State the blood parasite species.
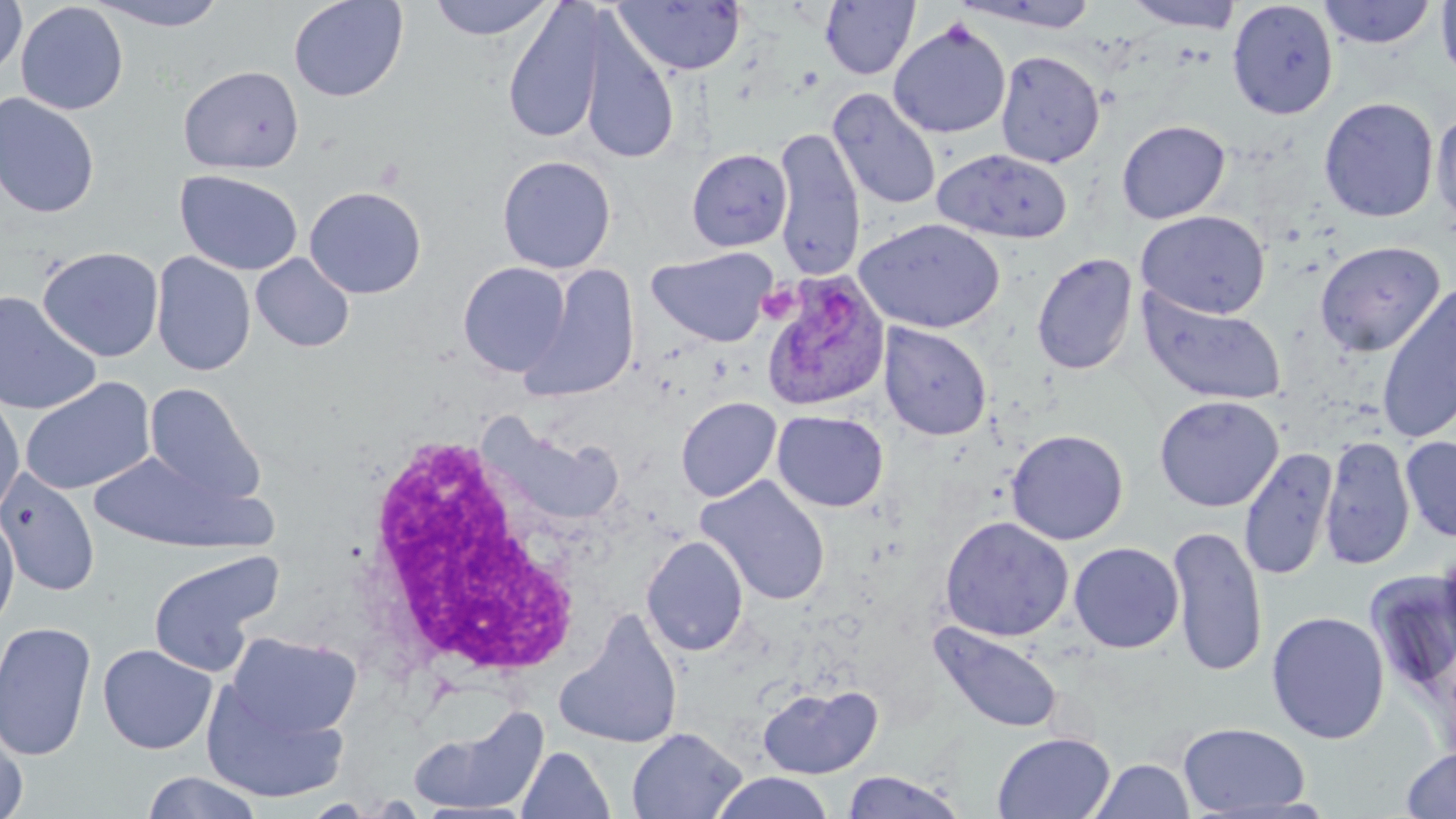

Plasmodium ovale.

{
  "magnification": "1000x",
  "modality": "optical microscopy",
  "field_of_view": "single",
  "preparation": "thin blood film",
  "stain": "May-Grünwald-Giemsa",
  "uninfected_red_blood_cell_locations": "approximate bounding boxes as named x1/y1/x2/y2 corners in pixels: (x1=0, y1=0, x2=27, y2=81), (x1=89, y1=0, x2=230, y2=32), (x1=288, y1=0, x2=409, y2=102), (x1=427, y1=0, x2=556, y2=40), (x1=612, y1=0, x2=746, y2=76), (x1=1123, y1=0, x2=1243, y2=31), (x1=1318, y1=0, x2=1436, y2=49), (x1=15, y1=1, x2=129, y2=116), (x1=820, y1=1, x2=920, y2=80), (x1=954, y1=1, x2=1101, y2=33), (x1=1227, y1=1, x2=1338, y2=119), (x1=1435, y1=1, x2=1456, y2=84), (x1=502, y1=2, x2=608, y2=145), (x1=578, y1=15, x2=681, y2=166), (x1=888, y1=20, x2=1011, y2=139), (x1=995, y1=50, x2=1105, y2=168), (x1=178, y1=65, x2=304, y2=174), (x1=828, y1=88, x2=941, y2=211), (x1=0, y1=93, x2=100, y2=219), (x1=1319, y1=96, x2=1439, y2=223), (x1=1432, y1=107, x2=1456, y2=231), (x1=1117, y1=120, x2=1230, y2=224), (x1=772, y1=128, x2=865, y2=279), (x1=686, y1=148, x2=792, y2=252), (x1=932, y1=148, x2=1073, y2=244), (x1=497, y1=155, x2=616, y2=274), (x1=174, y1=170, x2=303, y2=276), (x1=304, y1=185, x2=427, y2=299), (x1=1136, y1=210, x2=1270, y2=319), (x1=855, y1=218, x2=1005, y2=334), (x1=1315, y1=240, x2=1444, y2=358), (x1=37, y1=246, x2=164, y2=362), (x1=646, y1=247, x2=777, y2=347), (x1=151, y1=252, x2=256, y2=377), (x1=250, y1=253, x2=355, y2=352), (x1=1032, y1=253, x2=1138, y2=376), (x1=458, y1=261, x2=571, y2=378), (x1=522, y1=266, x2=640, y2=400), (x1=1376, y1=282, x2=1456, y2=445), (x1=1137, y1=289, x2=1287, y2=406), (x1=0, y1=292, x2=102, y2=415), (x1=879, y1=323, x2=992, y2=441), (x1=20, y1=377, x2=156, y2=495), (x1=143, y1=383, x2=266, y2=504), (x1=0, y1=390, x2=25, y2=518), (x1=1154, y1=395, x2=1283, y2=512), (x1=675, y1=397, x2=782, y2=502), (x1=772, y1=410, x2=889, y2=511), (x1=494, y1=427, x2=626, y2=525), (x1=1006, y1=429, x2=1129, y2=545), (x1=1319, y1=435, x2=1415, y2=571), (x1=1400, y1=436, x2=1456, y2=542), (x1=1238, y1=447, x2=1338, y2=582), (x1=89, y1=452, x2=267, y2=552), (x1=0, y1=468, x2=101, y2=597), (x1=695, y1=475, x2=831, y2=606), (x1=0, y1=509, x2=20, y2=634), (x1=939, y1=516, x2=1074, y2=642), (x1=1167, y1=525, x2=1268, y2=677), (x1=641, y1=535, x2=749, y2=657), (x1=1069, y1=542, x2=1184, y2=653), (x1=149, y1=550, x2=283, y2=678), (x1=1367, y1=569, x2=1456, y2=680), (x1=1266, y1=611, x2=1389, y2=745), (x1=555, y1=612, x2=684, y2=749), (x1=0, y1=621, x2=98, y2=762), (x1=930, y1=622, x2=1063, y2=734), (x1=226, y1=631, x2=363, y2=739), (x1=98, y1=644, x2=217, y2=754), (x1=758, y1=683, x2=883, y2=779), (x1=201, y1=684, x2=349, y2=803), (x1=408, y1=703, x2=549, y2=816), (x1=1178, y1=722, x2=1311, y2=815), (x1=0, y1=724, x2=29, y2=819), (x1=626, y1=727, x2=747, y2=819), (x1=992, y1=731, x2=1115, y2=818), (x1=516, y1=746, x2=615, y2=819), (x1=1399, y1=747, x2=1456, y2=818), (x1=1088, y1=758, x2=1195, y2=819), (x1=840, y1=770, x2=967, y2=818), (x1=141, y1=771, x2=264, y2=819), (x1=710, y1=772, x2=835, y2=818)",
  "white_blood_cell_locations": "approximate bounding boxes as named x1/y1/x2/y2 corners in pixels: (x1=360, y1=433, x2=591, y2=685)",
  "plasmodium_ovale_infected_red_blood_cell_locations": "approximate bounding boxes as named x1/y1/x2/y2 corners in pixels: (x1=759, y1=272, x2=890, y2=413)",
  "image_size": "1456×819 pixels"
}